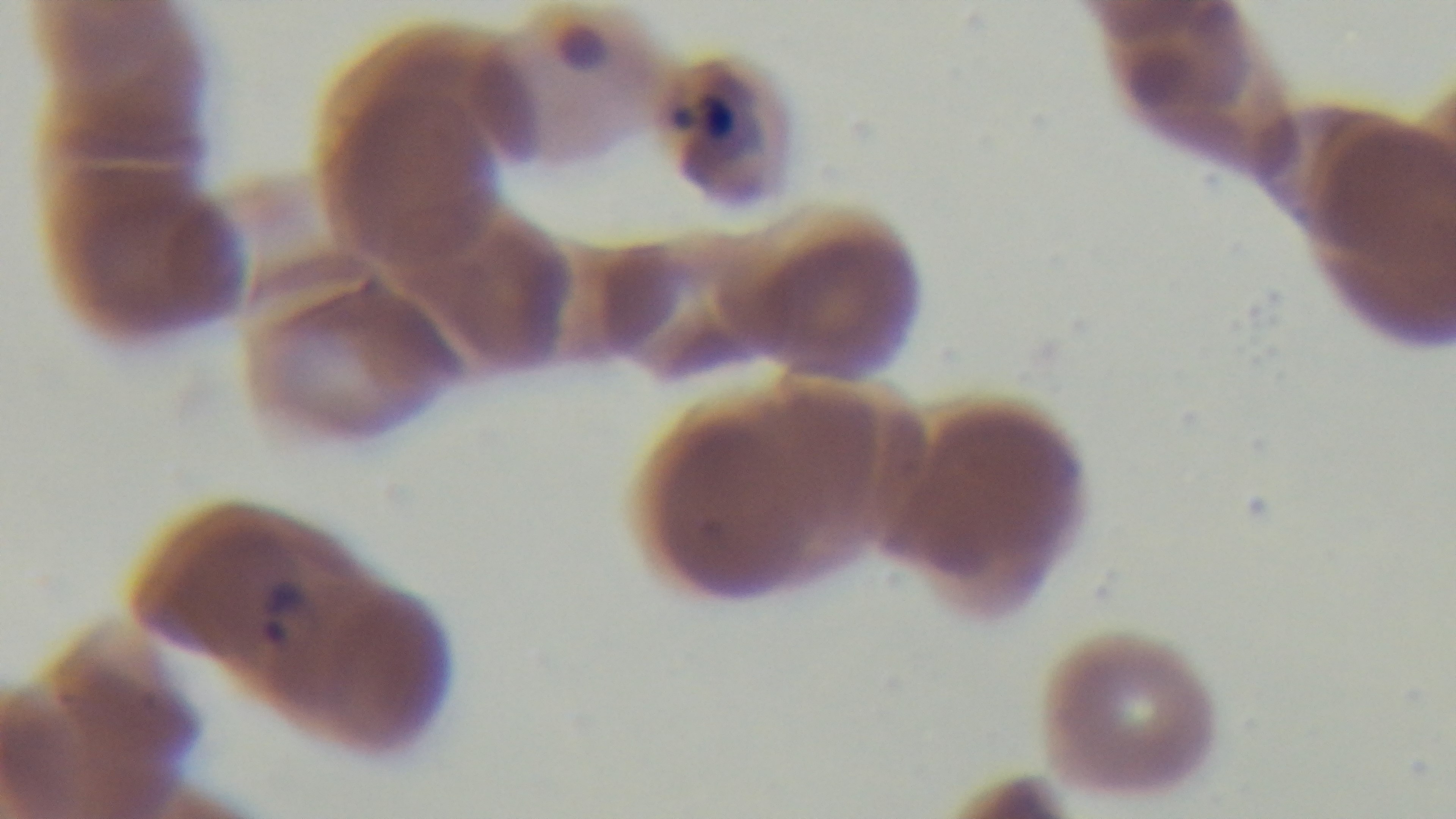

capture = mounted 4K digital camera
stain = Giemsa
preparation = thin smear
objective = 100x oil immersion
field of view = one from the slide
modality = light microscopy
malaria status = infected